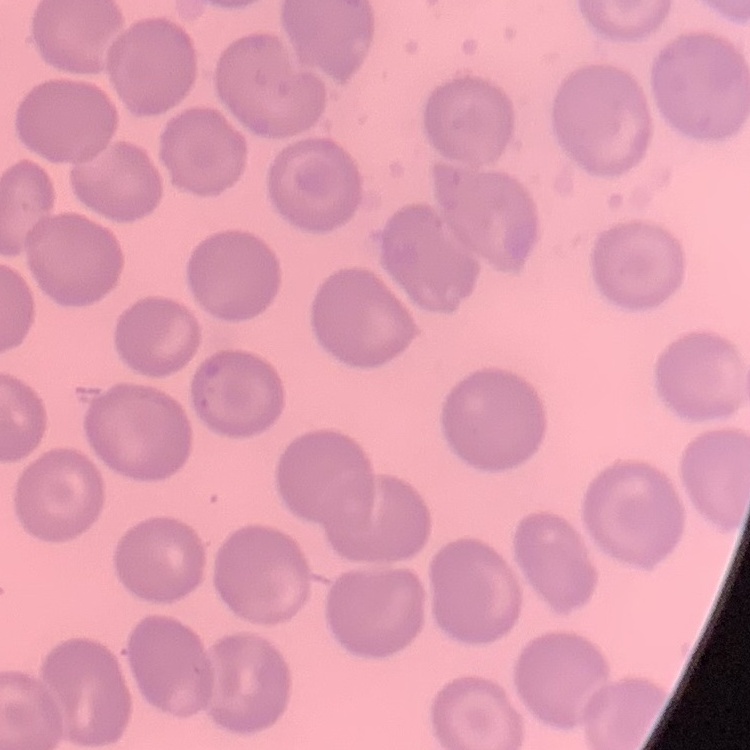
Summary:
  - Erythrocyte morphology: no rouleaux formation
  - Preparation: thin blood film
  - Image type: one tile cut from a larger photomicrograph
  - Stain: Field's or Giemsa